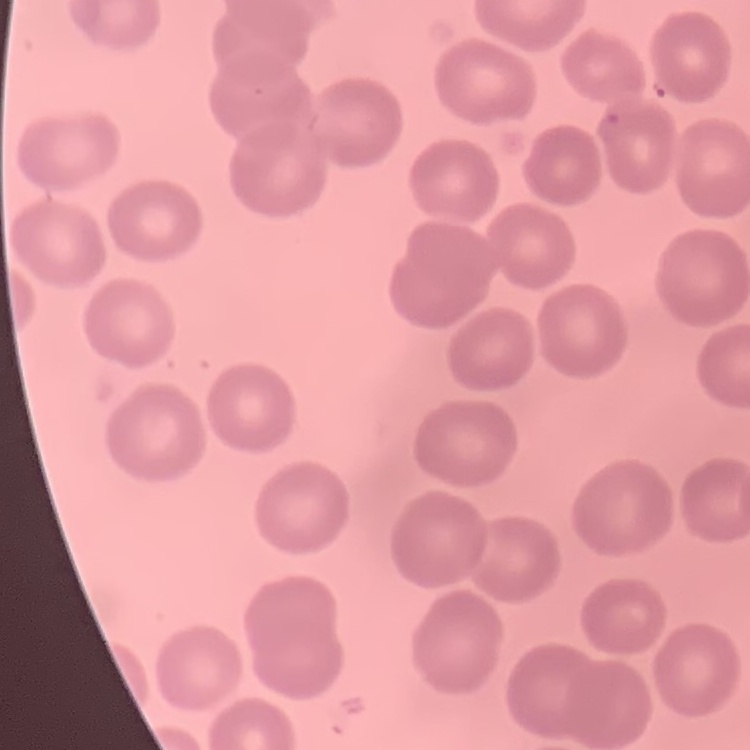

Summary:
  - Erythrocyte morphology: no rouleaux formation
  - Image type: one tile cut from a larger photomicrograph
  - Preparation: thin blood film
  - Stain: Field's or Giemsa